State which cell type is depicted.
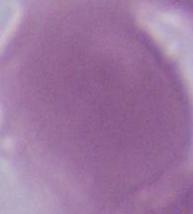
This is an erythrocyte.

Summary:
  - Magnification: 1000x
  - Modality: micrograph